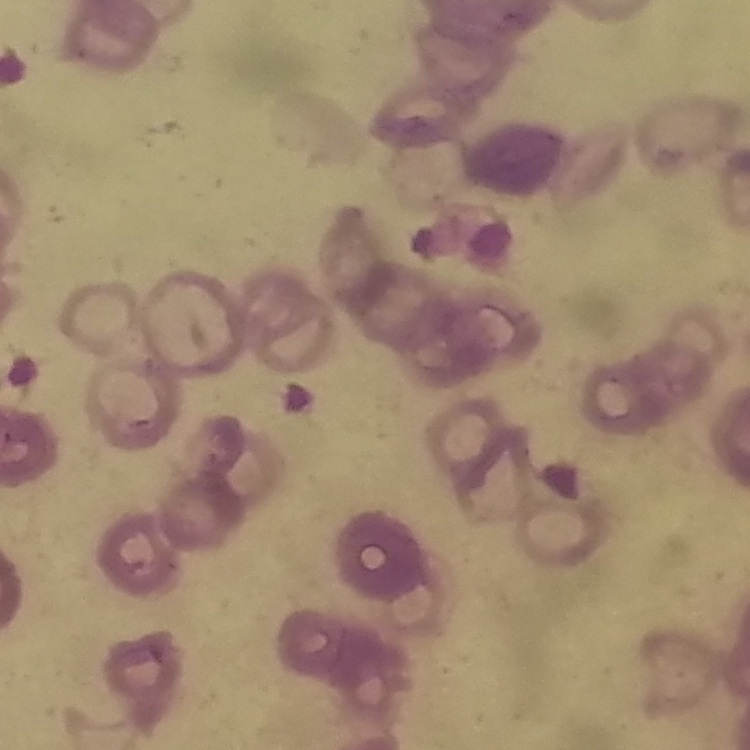 The red blood cells exhibit rouleaux formation. Stained with either Field's or Giemsa. One tile cut from a larger photomicrograph. Thin blood film.